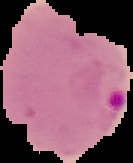 From a thin blood smear. Cell region segmented out of the field of view; the surrounding area is masked to black. Result: malaria parasites identified. Image is 133×163 pixels.